Report the malaria status of this cell.
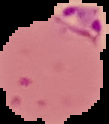
Parasitized.

From a thin blood smear. Cell region segmented out of the field of view; the surrounding area is masked to black. Image is 109×124 pixels.